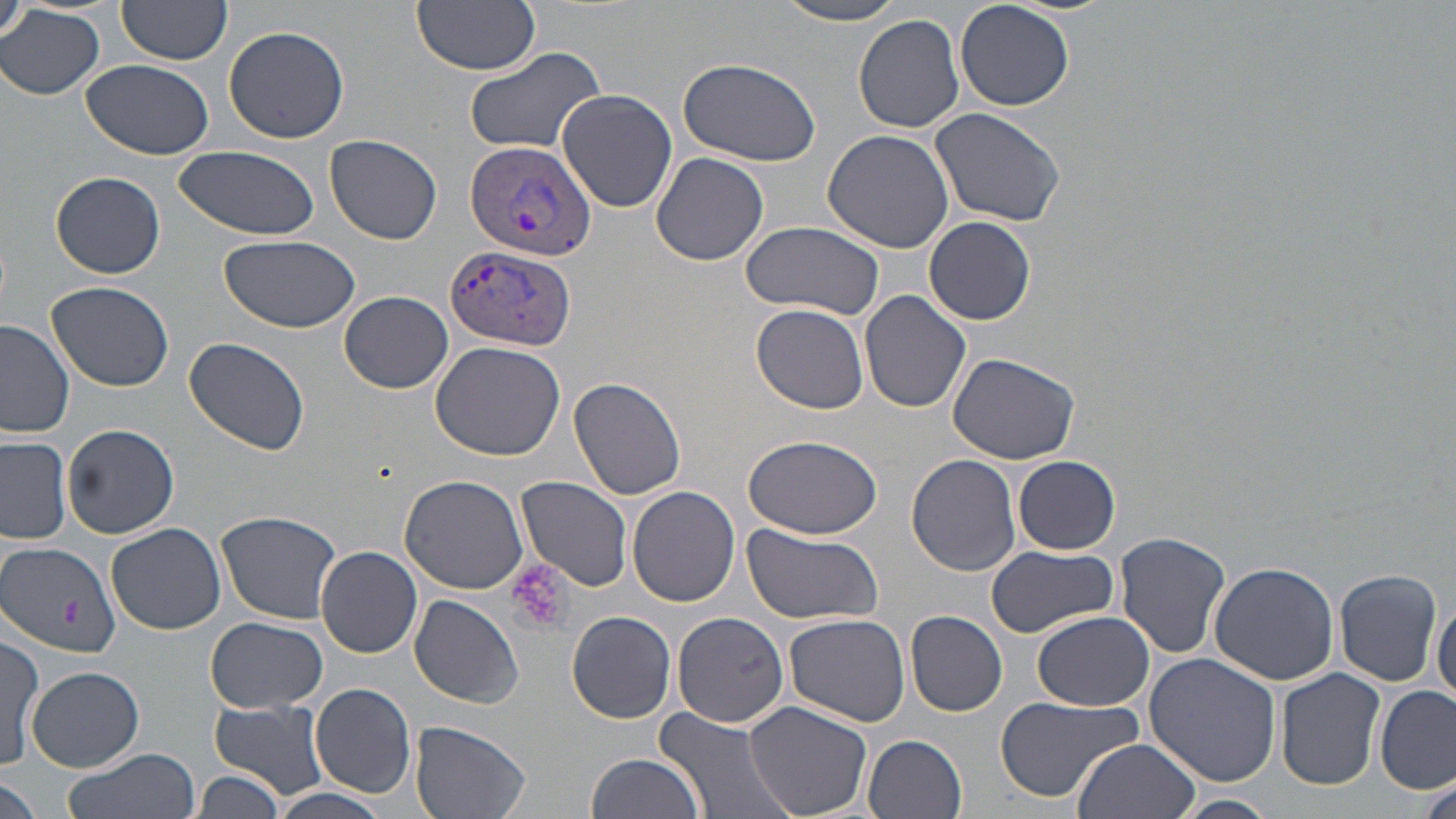

slide-level diagnosis = Plasmodium vivax
stain = May-Grünwald-Giemsa
uninfected red blood cell locations = approximate bounding boxes as named x1/y1/x2/y2 corners in pixels: (x1=3, y1=0, x2=31, y2=46), (x1=413, y1=0, x2=540, y2=74), (x1=773, y1=0, x2=913, y2=25), (x1=955, y1=0, x2=1076, y2=111), (x1=117, y1=1, x2=232, y2=68), (x1=0, y1=4, x2=104, y2=99), (x1=852, y1=14, x2=967, y2=134), (x1=223, y1=24, x2=350, y2=145), (x1=464, y1=46, x2=607, y2=156), (x1=676, y1=57, x2=823, y2=166), (x1=80, y1=58, x2=214, y2=160), (x1=555, y1=88, x2=677, y2=213), (x1=930, y1=106, x2=1067, y2=226), (x1=822, y1=129, x2=954, y2=252), (x1=325, y1=135, x2=442, y2=245), (x1=172, y1=146, x2=321, y2=238), (x1=651, y1=152, x2=769, y2=266), (x1=50, y1=171, x2=166, y2=279), (x1=924, y1=216, x2=1035, y2=326), (x1=739, y1=221, x2=884, y2=320), (x1=220, y1=235, x2=362, y2=333), (x1=45, y1=282, x2=174, y2=393), (x1=859, y1=289, x2=973, y2=414), (x1=340, y1=291, x2=453, y2=394), (x1=752, y1=304, x2=870, y2=415), (x1=0, y1=320, x2=75, y2=438), (x1=185, y1=337, x2=312, y2=458), (x1=430, y1=340, x2=565, y2=460), (x1=947, y1=352, x2=1081, y2=464), (x1=567, y1=376, x2=687, y2=502), (x1=62, y1=425, x2=179, y2=538), (x1=741, y1=434, x2=882, y2=540), (x1=0, y1=436, x2=72, y2=546), (x1=906, y1=454, x2=1021, y2=575), (x1=1013, y1=455, x2=1121, y2=555), (x1=400, y1=472, x2=532, y2=594), (x1=517, y1=476, x2=634, y2=592), (x1=628, y1=486, x2=740, y2=606), (x1=216, y1=510, x2=344, y2=623), (x1=741, y1=523, x2=884, y2=627), (x1=108, y1=524, x2=227, y2=636), (x1=1114, y1=531, x2=1233, y2=661), (x1=1, y1=543, x2=121, y2=657), (x1=983, y1=545, x2=1120, y2=638), (x1=316, y1=547, x2=422, y2=658), (x1=1207, y1=560, x2=1339, y2=684), (x1=1334, y1=566, x2=1444, y2=686), (x1=409, y1=594, x2=524, y2=708), (x1=1432, y1=596, x2=1455, y2=710), (x1=566, y1=609, x2=677, y2=723), (x1=672, y1=610, x2=791, y2=729), (x1=905, y1=610, x2=1008, y2=716), (x1=1030, y1=610, x2=1155, y2=712), (x1=783, y1=613, x2=912, y2=727), (x1=203, y1=616, x2=328, y2=713), (x1=1, y1=632, x2=42, y2=770), (x1=1143, y1=654, x2=1283, y2=789), (x1=27, y1=666, x2=143, y2=771), (x1=1276, y1=670, x2=1387, y2=789), (x1=309, y1=684, x2=416, y2=798), (x1=1375, y1=686, x2=1455, y2=795), (x1=992, y1=694, x2=1140, y2=802), (x1=209, y1=700, x2=329, y2=801), (x1=743, y1=700, x2=875, y2=819), (x1=654, y1=707, x2=798, y2=819), (x1=408, y1=720, x2=533, y2=819), (x1=862, y1=734, x2=968, y2=819), (x1=1072, y1=738, x2=1201, y2=819), (x1=64, y1=747, x2=200, y2=819), (x1=584, y1=753, x2=705, y2=819), (x1=197, y1=771, x2=285, y2=818), (x1=0, y1=774, x2=41, y2=819), (x1=1418, y1=774, x2=1455, y2=819), (x1=269, y1=786, x2=397, y2=819), (x1=1171, y1=794, x2=1281, y2=819)
image size = 1456×819 pixels
preparation = thin blood smear
field of view = one of a larger specimen
platelet locations = approximate bounding boxes as named x1/y1/x2/y2 corners in pixels: (x1=507, y1=560, x2=572, y2=636), (x1=62, y1=599, x2=80, y2=631)
modality = optical microscopy
Plasmodium vivax-infected red blood cell locations = approximate bounding boxes as named x1/y1/x2/y2 corners in pixels: (x1=464, y1=140, x2=595, y2=261), (x1=443, y1=244, x2=575, y2=352)
magnification = 1000x